Give the position of every malaria parasite.
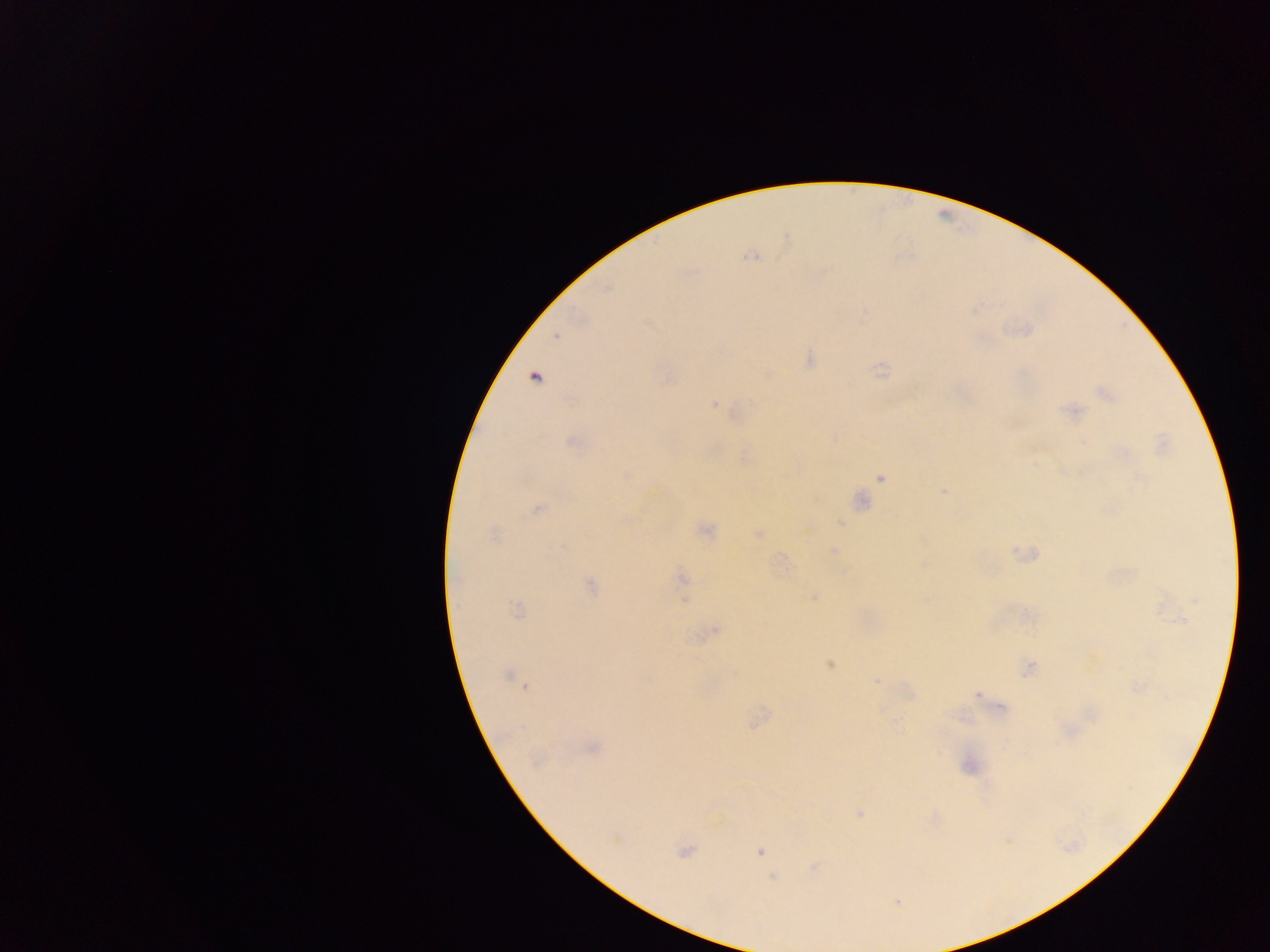

Approximate centers as [x, y] in pixels.
Malaria parasites: [751, 256], [556, 336], [535, 378], [1106, 394], [715, 404], [1071, 411], [574, 443], [626, 475], [881, 478], [944, 491], [861, 501], [537, 509], [706, 530], [759, 534], [493, 535], [563, 546], [835, 549], [925, 564], [683, 578], [591, 585], [814, 597], [516, 609], [1180, 621], [716, 629], [829, 664], [1029, 668], [507, 676], [876, 681], [525, 687], [977, 695], [1002, 708], [592, 747], [860, 813], [615, 841], [684, 851], [759, 851], [897, 902].

Thick blood film. Collected in Ghana. Photographed through a microscope with a mobile-phone camera. One field of view. Image is 1270×952 pixels.